Give a bounding box for every Plasmodium parasite.
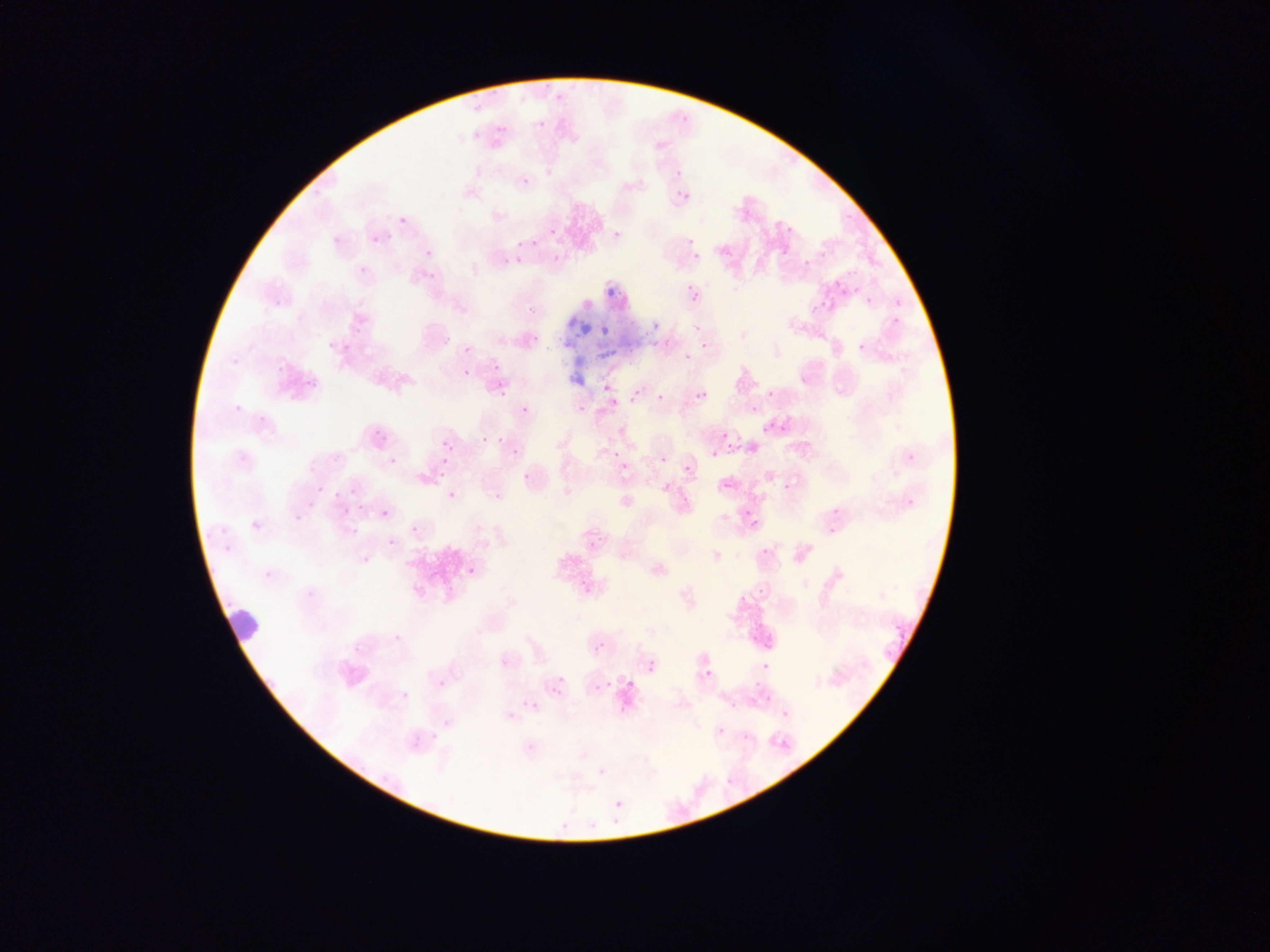
Approximate bounding boxes as left top right bottom in pixels.
Plasmodium parasites: 677 103 705 124; 538 119 546 129; 496 125 506 135; 471 131 480 141; 671 164 688 174; 521 176 531 187; 678 190 690 202; 399 217 408 226; 781 220 799 233; 548 227 558 237; 612 228 623 241; 331 234 342 246; 370 235 380 245; 423 237 438 256; 532 240 540 248; 516 241 524 249; 692 245 700 264; 781 246 790 256; 692 252 701 261; 799 253 809 266; 515 256 524 265; 425 258 440 278; 357 264 372 279; 686 283 699 296; 837 285 847 295; 686 286 703 304; 814 293 831 311; 866 295 875 308; 889 315 900 328; 651 320 663 333; 532 326 547 339; 601 326 611 337; 322 327 339 349; 699 339 713 351; 856 341 868 353; 341 342 352 354; 462 345 472 355; 492 350 507 368; 684 352 693 362; 225 353 241 366; 275 359 289 373; 462 369 472 379; 303 376 317 392; 598 380 613 393; 494 382 516 397; 764 389 777 397; 697 390 708 402; 631 391 642 403; 656 394 665 402; 516 398 532 413; 235 405 250 414; 750 405 759 415; 577 406 586 415; 257 408 269 426; 761 418 777 435; 374 430 388 445; 477 430 489 448; 722 433 731 443; 493 436 508 445; 442 439 452 450; 509 443 522 456; 238 445 252 460; 612 449 622 460; 660 455 668 464; 390 456 401 469; 440 457 449 468; 433 459 453 486; 620 461 631 472; 684 465 692 474; 520 470 534 484; 723 479 735 491; 498 480 516 496; 782 481 794 495; 316 486 324 495; 334 490 344 499; 447 490 459 503; 902 493 920 512; 344 503 353 518; 741 504 756 518; 354 509 366 516; 381 509 391 519; 294 513 303 523; 746 514 764 532; 221 518 232 532; 824 519 840 535; 411 525 422 537; 387 537 397 547; 224 546 235 559; 760 546 771 557; 467 566 478 579; 579 571 595 586; 760 585 768 595; 736 593 751 603; 391 624 405 640; 748 634 759 645; 596 640 607 652; 880 644 899 663; 759 656 773 673; 647 662 659 676; 702 667 715 682; 436 672 452 692; 752 679 761 685; 603 680 613 690; 596 682 606 693; 552 685 564 698; 398 690 416 702; 761 693 771 712; 528 698 542 712; 777 707 790 719; 506 711 518 723; 715 726 726 737; 740 728 752 742; 414 730 425 743; 779 735 800 758; 596 765 607 778; 718 781 731 791; 612 798 624 811 | approximate x y pixel centers of objects too small to bound: 856 289; 714 455.

preparation = thin blood smear
image size = 1270×952 pixels
country = Ghana
leukocyte locations = approximate bounding boxes as left top right bottom in pixels: 229 601 270 645
field of view = single
capture = mobile-phone photograph through a microscope